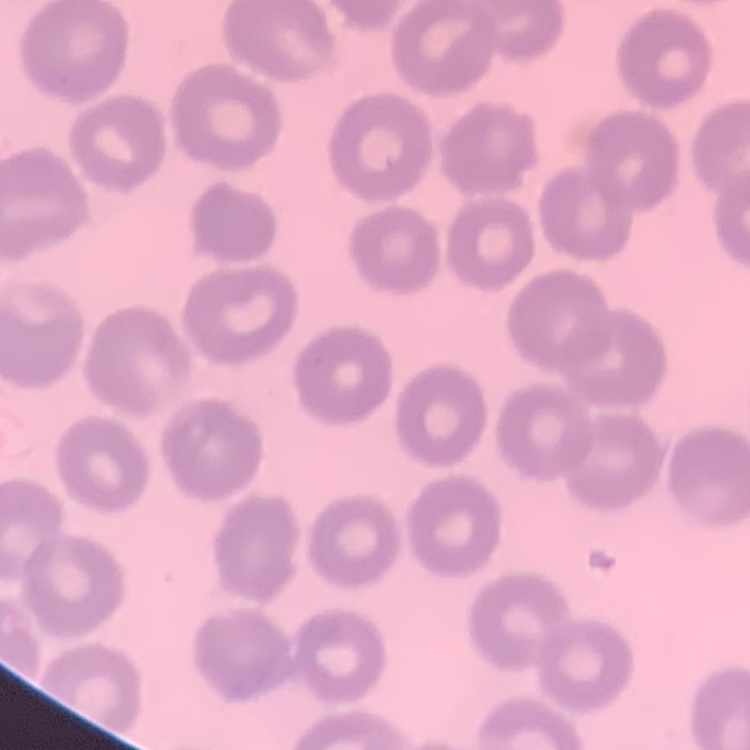

Summary:
  - Erythrocyte morphology: no rouleaux formation
  - Preparation: thin peripheral smear
  - Stain: Field's or Giemsa
  - Image type: one tile cut from a larger photomicrograph